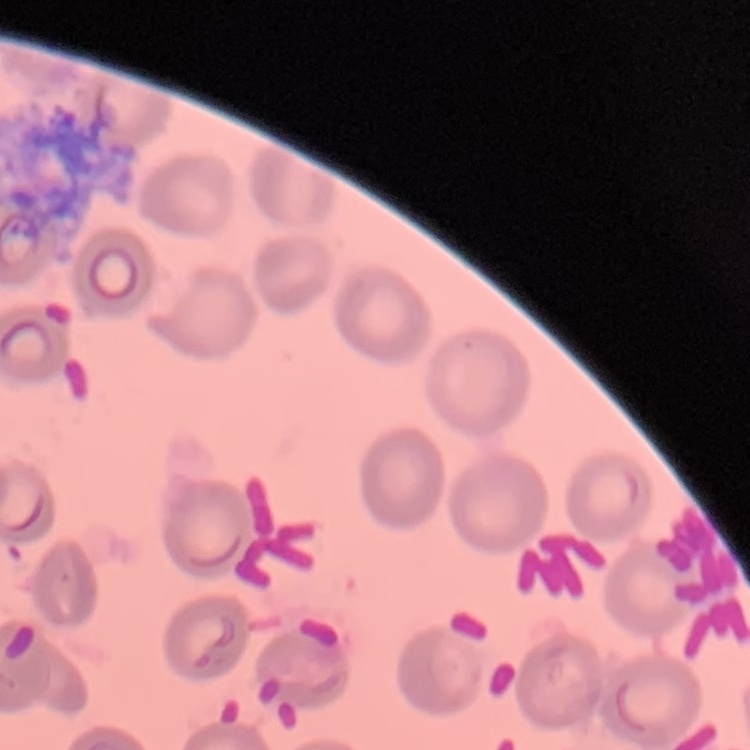
red blood cell morphology = no rouleaux formation
preparation = thin peripheral smear
image type = one tile cut from a larger photomicrograph
stain = Field's or Giemsa